Assess the morphology of the erythrocytes.
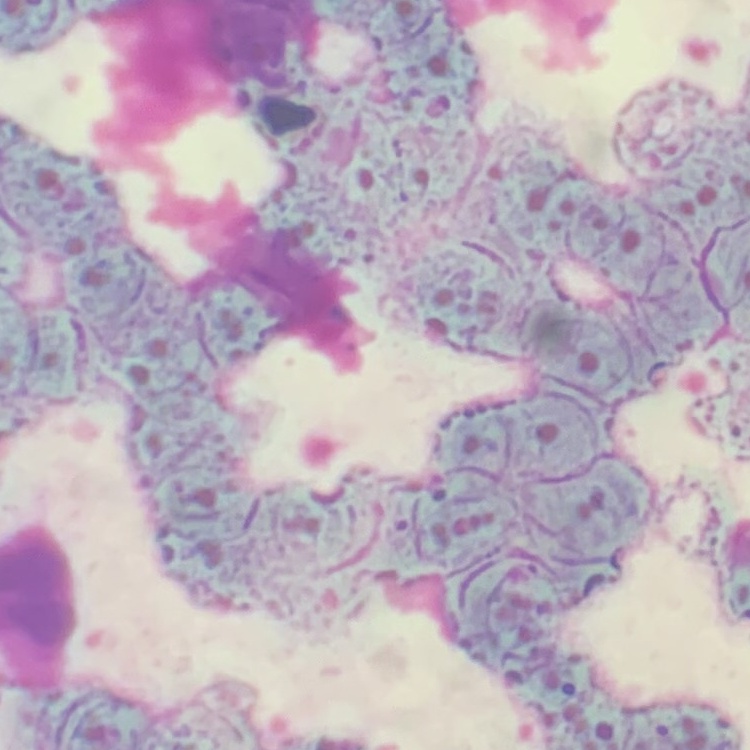

They show rouleaux formation.

Square crop of a larger photomicrograph. Thin blood film. Field's or Giemsa stain.